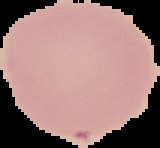

image size = 160×148 pixels
preparation = thin blood film
image type = segmented cell region with the area outside set to black
malaria status = uninfected